Point out each leukocyte.
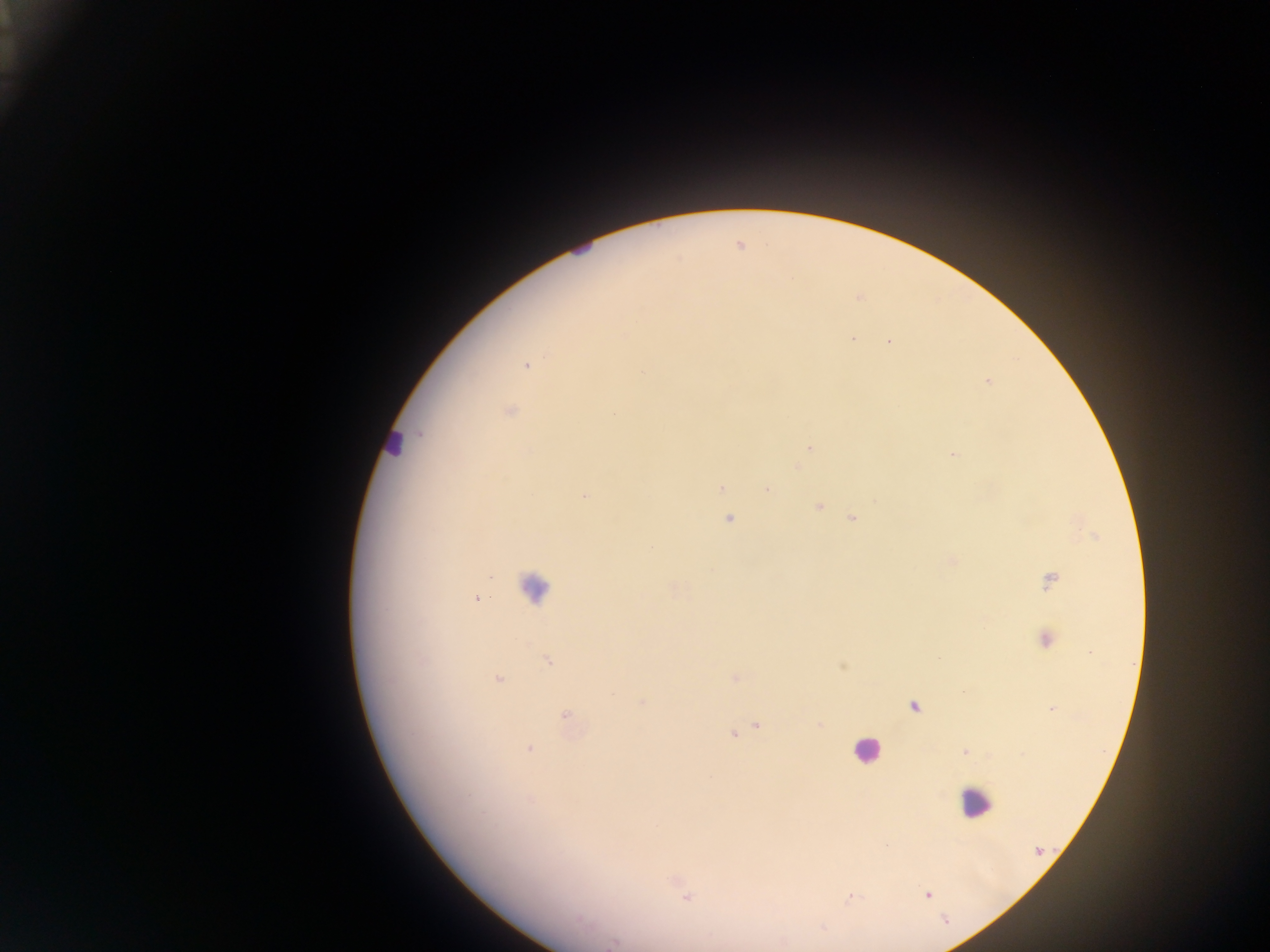

Approximate centers as [x, y] in pixels.
Leukocytes: [580, 246], [393, 443], [535, 587], [866, 749], [974, 803].

Summary:
  - Malaria parasite locations: [853, 339], [889, 342], [525, 366], [642, 372], [987, 381], [510, 412], [809, 448], [954, 454], [721, 488], [767, 489], [584, 496], [819, 507], [728, 518], [851, 519], [1050, 581], [476, 598], [1046, 638], [548, 660], [735, 678], [498, 679], [642, 702], [914, 707], [566, 715], [757, 725], [732, 734], [529, 748], [965, 752], [531, 800], [1039, 852], [926, 895], [686, 897], [945, 920], [613, 942]
  - Preparation: thick blood film
  - Image size: 1270×952 pixels
  - Capture: mobile-phone photograph through a microscope
  - Field of view: single
  - Country: Ghana